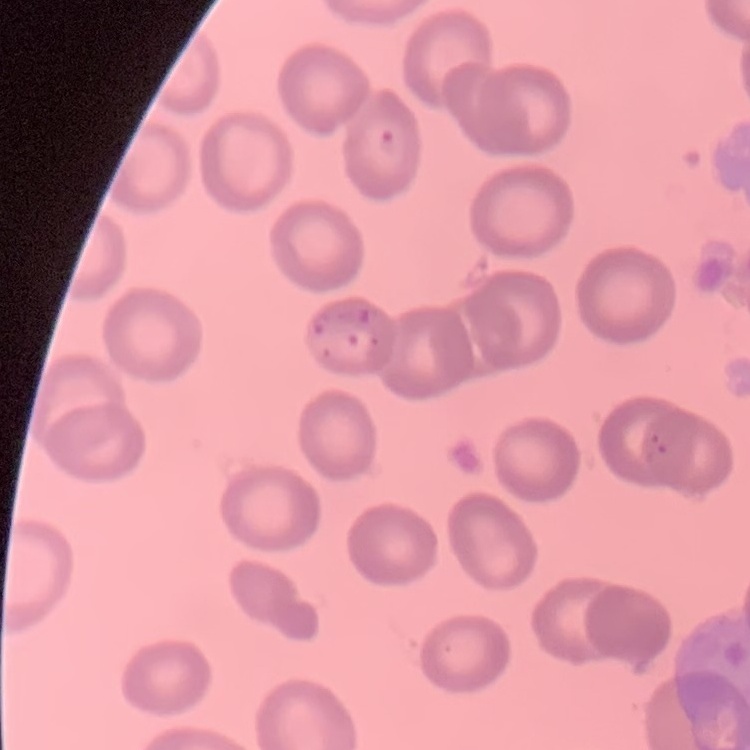
The red blood cells show no rouleaux formation. One tile cut from a larger photomicrograph. Stained with either Field's or Giemsa. Thin peripheral smear.